Comment on the morphology of the red blood cells.
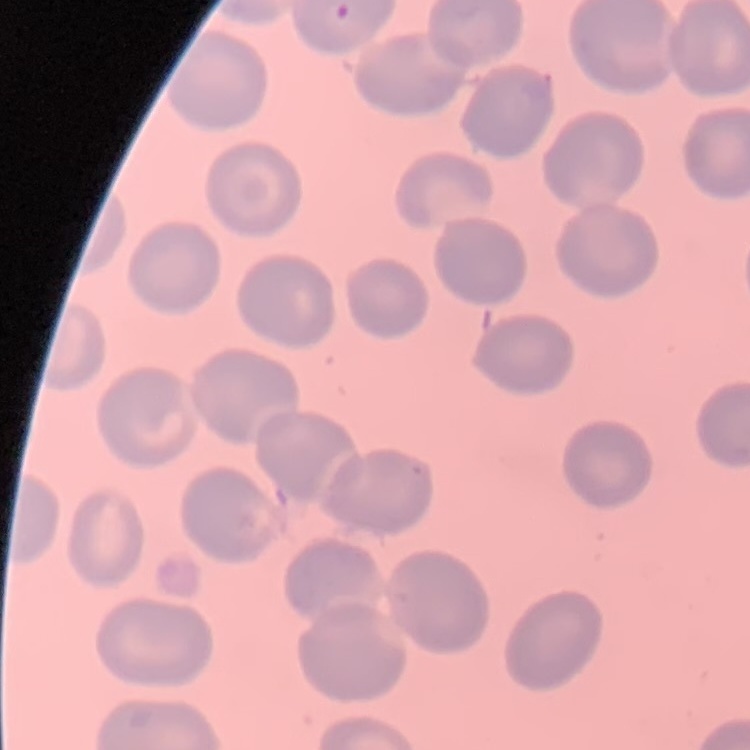
They show no rouleaux formation.

preparation = thin blood film
image type = one tile cut from a larger photomicrograph
stain = Field's or Giemsa